Describe the morphology of the erythrocytes.
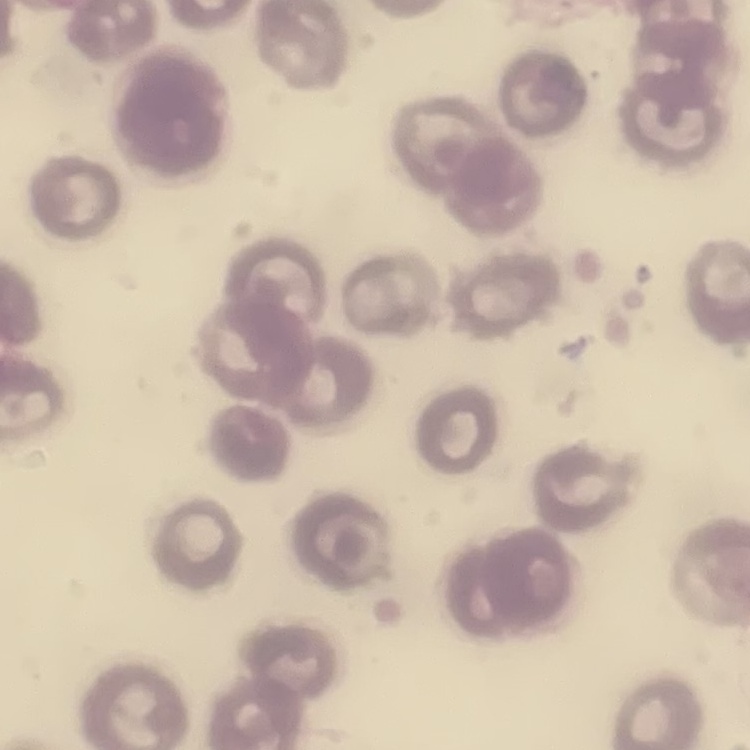

No rouleaux formation.

Thin peripheral smear. Stained with either Field's or Giemsa. One tile cut from a larger photomicrograph.